Identify the parasite.
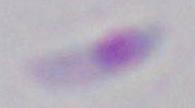
Toxoplasma gondii.

magnification = 1000x
modality = photomicrograph